Give the position of every leukocyte visible.
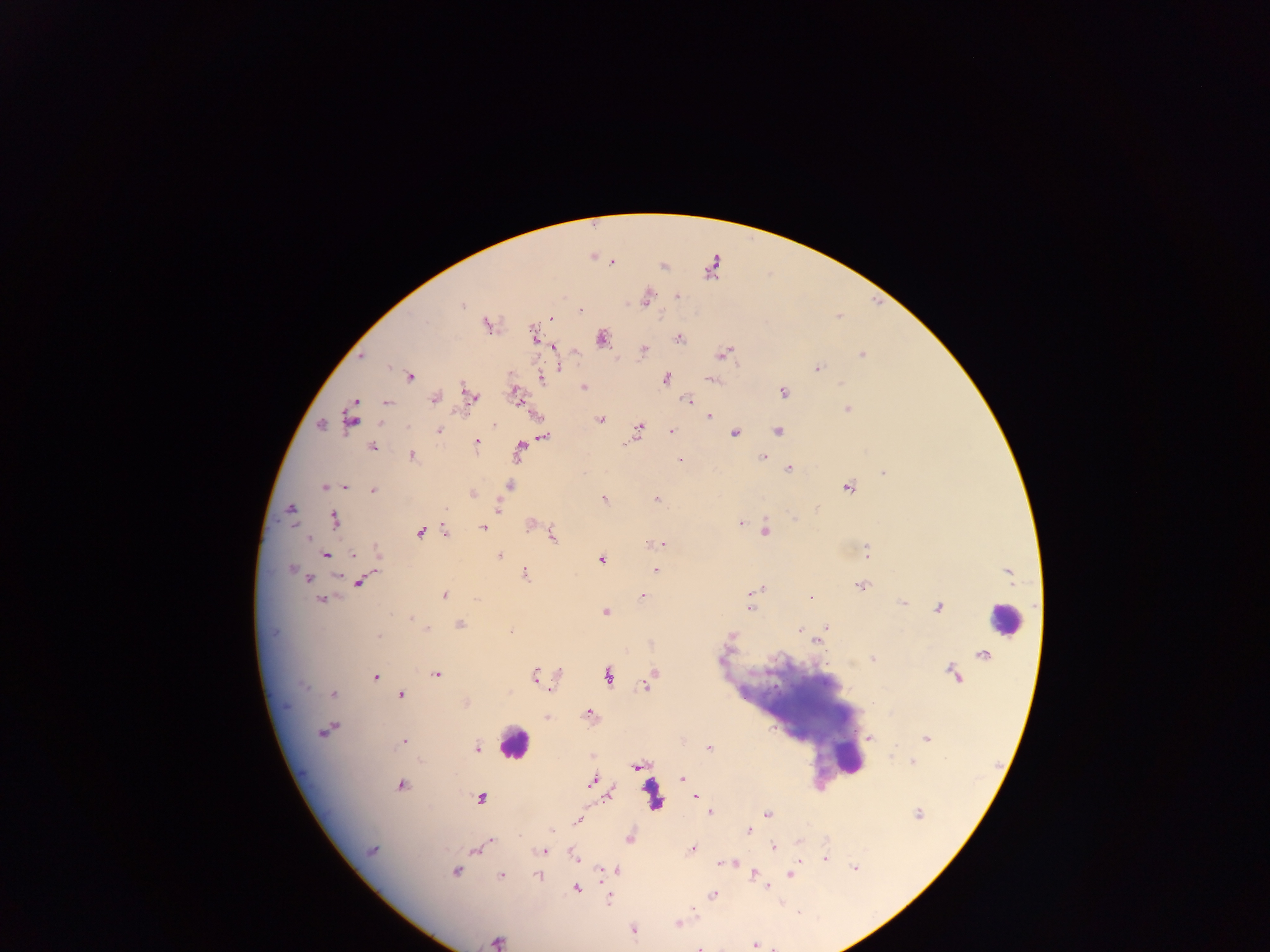
Approximate centers as x y in pixels.
Leukocytes: 1003 619; 515 742; 846 757; 655 794.

Plasmodium parasite locations = approximate centers as x y in pixels: 612 263; 664 267; 676 295; 646 299; 462 305; 581 310; 551 319; 486 326; 533 337; 602 338; 679 339; 553 346; 644 349; 724 354; 861 355; 362 356; 559 366; 817 368; 409 377; 665 378; 542 379; 712 380; 842 383; 584 387; 465 388; 783 392; 516 394; 471 396; 434 398; 687 400; 386 402; 848 410; 708 416; 350 418; 601 419; 321 425; 382 425; 408 426; 639 429; 439 430; 671 431; 777 431; 735 433; 544 436; 477 442; 625 443; 372 447; 520 448; 412 456; 763 458; 680 460; 789 468; 884 474; 509 485; 322 486; 346 487; 848 488; 373 491; 472 494; 657 498; 604 499; 498 507; 446 508; 291 509; 335 519; 795 519; 530 524; 740 524; 483 528; 765 530; 446 532; 419 533; 553 537; 308 538; 663 545; 379 553; 867 554; 325 555; 353 555; 500 556; 601 559; 291 570; 655 571; 524 574; 303 575; 337 577; 307 578; 360 581; 860 587; 762 589; 445 595; 643 596; 811 598; 321 601; 903 603; 749 608; 938 608; 605 611; 411 618; 460 624; 826 627; 427 628; 799 630; 510 631; 731 635; 379 636; 815 641; 872 659; 559 673; 436 674; 654 674; 375 675; 534 675; 607 676; 645 685; 304 686; 333 695; 401 695; 465 702; 589 713; 548 717; 323 732; 870 738; 926 738; 404 742; 478 748; 709 748; 891 756; 913 762; 636 767; 682 779; 592 782; 401 785; 610 795; 696 796; 480 798; 710 811; 767 814; 918 814; 577 821; 552 830; 748 831; 630 838; 799 842; 488 844; 773 847; 692 849; 372 850; 475 850; 542 850; 574 857; 825 860; 800 861; 734 863; 719 864; 854 868; 602 869; 616 870; 456 872; 754 873; 501 875; 537 875; 790 875; 767 887; 577 889; 712 895; 609 898; 678 922; 633 930; 497 940; 754 945; 700 948
capture = mobile-phone photograph through a microscope
preparation = thick blood film
field of view = single
image size = 1270×952 pixels
country = Ghana